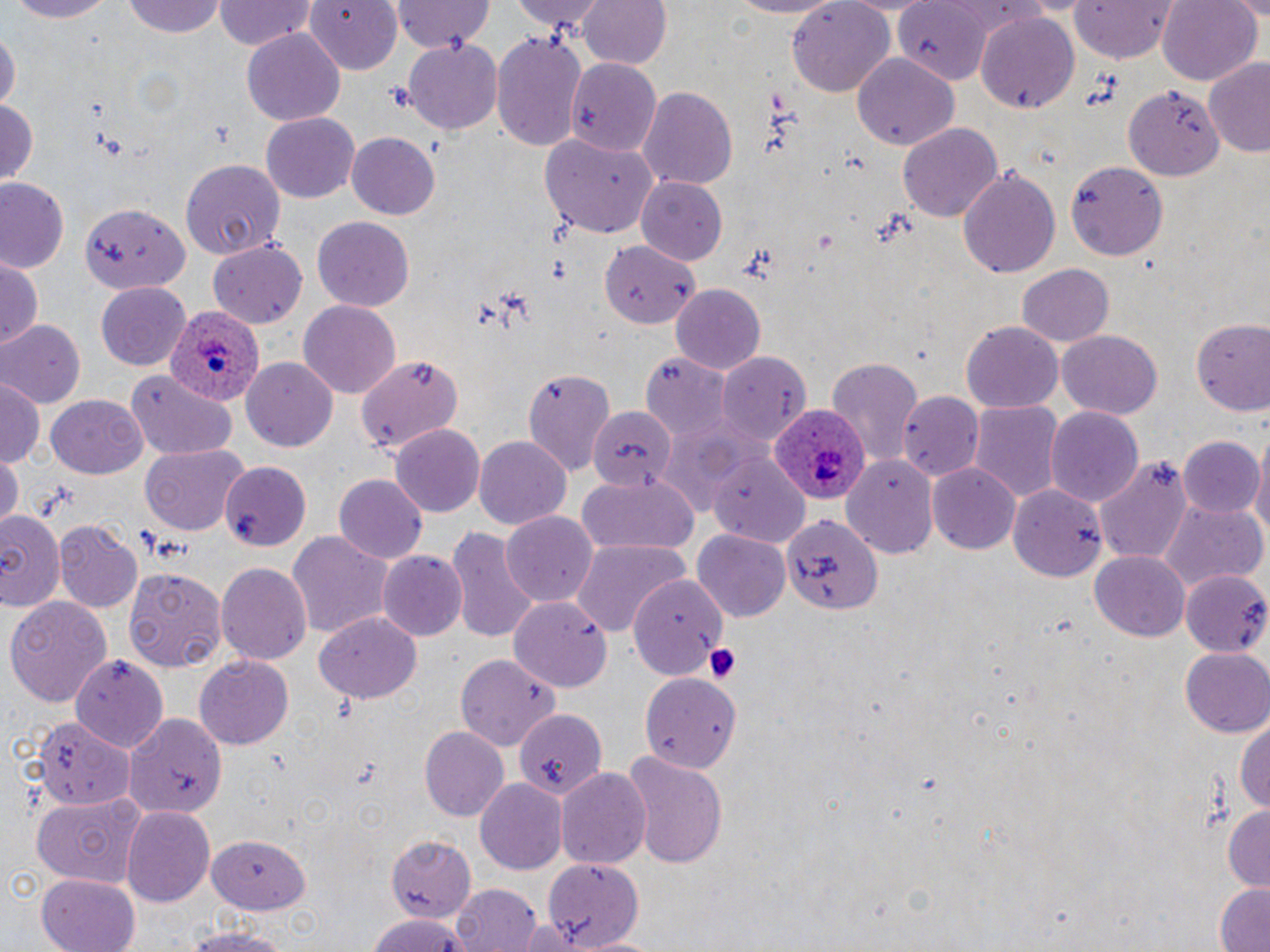
slide_level_diagnosis: Plasmodium ovale
magnification: 1000x
stain: May-Grünwald-Giemsa
platelet_locations: 'approximate bounding boxes as (x1, y1, x2, y2) in pixels: (703, 642, 743, 686)'
uninfected_red_blood_cell_locations: 'approximate bounding boxes as (x1, y1, x2, y2) in pixels: (0, 0, 119, 23), (124, 0, 229, 38), (301, 0, 404, 75), (514, 0, 609, 35), (578, 0, 671, 71), (721, 0, 851, 19), (1158, 0, 1261, 87), (214, 1, 314, 51), (391, 1, 493, 52), (896, 1, 991, 82), (1071, 1, 1179, 63), (787, 2, 894, 95), (974, 10, 1080, 117), (0, 28, 18, 117), (242, 28, 345, 124), (492, 32, 588, 154), (405, 36, 500, 135), (853, 54, 957, 150), (1204, 55, 1270, 158), (565, 58, 662, 154), (1124, 83, 1225, 181), (640, 85, 740, 192), (1, 94, 38, 189), (261, 113, 361, 203), (897, 123, 1003, 222), (346, 133, 440, 218), (542, 134, 658, 238), (179, 158, 282, 260), (1065, 159, 1166, 261), (957, 166, 1061, 278), (636, 177, 729, 265), (1, 179, 69, 273), (79, 199, 193, 294), (312, 217, 416, 311), (208, 240, 309, 331), (598, 240, 696, 324), (0, 257, 43, 349), (1018, 261, 1114, 346), (94, 280, 191, 371), (672, 284, 767, 376), (299, 298, 402, 397), (1193, 317, 1268, 421), (0, 320, 84, 409), (960, 321, 1063, 412), (1054, 329, 1162, 420), (717, 350, 811, 444), (355, 354, 462, 457), (645, 354, 734, 444), (243, 358, 338, 452), (828, 358, 921, 468), (525, 368, 618, 478), (124, 372, 238, 460), (1, 377, 42, 472), (899, 392, 984, 482), (45, 393, 149, 478), (968, 401, 1064, 504), (1044, 405, 1143, 510), (585, 406, 674, 492), (390, 424, 484, 519), (1251, 432, 1270, 546), (1182, 435, 1259, 518), (473, 436, 572, 528), (139, 444, 249, 534), (0, 451, 22, 528), (711, 452, 809, 544), (840, 453, 940, 558), (1093, 458, 1193, 564), (223, 461, 309, 549), (929, 462, 1020, 555), (578, 472, 700, 557), (334, 474, 427, 564), (1008, 481, 1106, 581), (1160, 503, 1265, 593), (0, 509, 63, 608), (502, 513, 598, 607), (782, 514, 884, 618), (54, 520, 141, 614), (446, 525, 541, 642), (692, 529, 791, 624), (287, 530, 395, 640), (570, 540, 686, 638), (377, 550, 466, 640), (1090, 551, 1190, 642), (216, 562, 310, 667), (124, 568, 227, 670), (1179, 571, 1270, 654), (630, 573, 722, 680), (5, 594, 111, 705), (512, 598, 612, 693), (316, 611, 424, 705), (1181, 649, 1270, 737), (457, 653, 559, 750), (72, 655, 171, 752), (196, 656, 294, 749), (642, 673, 742, 774), (513, 709, 608, 801), (1234, 711, 1270, 820), (124, 712, 224, 820), (34, 716, 134, 808), (421, 726, 510, 822), (620, 750, 729, 867), (556, 766, 654, 868), (474, 779, 567, 874), (31, 790, 147, 889), (121, 805, 215, 908), (1222, 806, 1269, 892), (209, 833, 311, 915), (388, 835, 477, 921), (543, 857, 645, 949), (37, 872, 138, 952), (451, 883, 543, 952), (1212, 884, 1270, 952), (364, 913, 473, 952), (518, 918, 582, 952), (172, 925, 295, 952)'
image_size: 1270×952 pixels
plasmodium_ovale_infected_red_blood_cell_locations: 'approximate bounding boxes as (x1, y1, x2, y2) in pixels: (169, 301, 264, 407), (771, 406, 867, 508)'
modality: optical microscopy
field_of_view: one of a larger specimen
preparation: thin blood film